Classify this cell by malaria status.
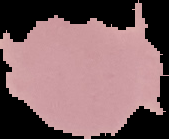

It is uninfected.

From a thin blood smear. Image is 169×139 pixels. Segmented cell region on a black background.